Report the malaria status of this cell.
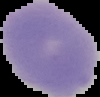

Uninfected.

{
  "image_type": "segmented cell region with the area outside set to black",
  "image_size": "100×97 pixels",
  "preparation": "thin blood smear"
}